Locate every Plasmodium parasite.
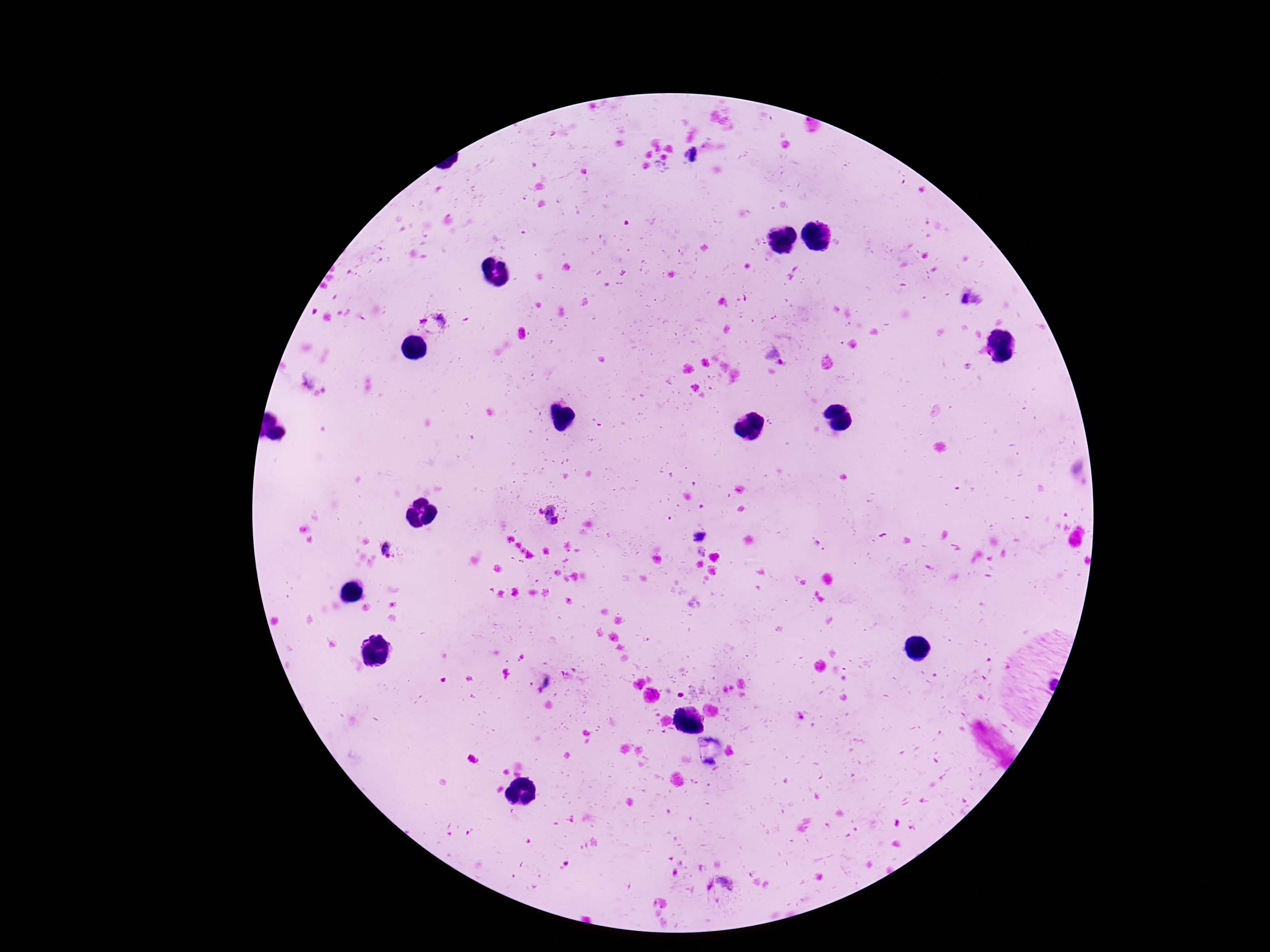
Approximate object centers, in pixels from the top-left corner.
Plasmodium parasites: (x=432, y=325), (x=775, y=356), (x=312, y=388), (x=551, y=515), (x=701, y=536), (x=387, y=550), (x=545, y=682), (x=724, y=884).

Summary:
  - Stain: Giemsa
  - Capture: smartphone camera through the microscope eyepiece
  - Magnification: 100x
  - Image size: 1270×952 pixels
  - Preparation: thick peripheral-blood smear
  - Patient malaria status: infected
  - Field of view: one from this slide